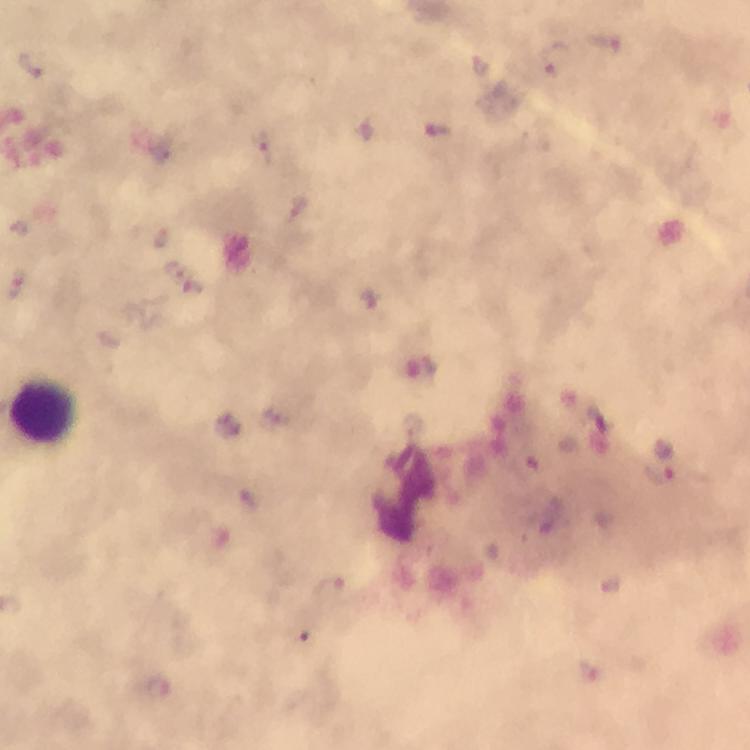

Approximate centers as (x, y) in pixels.
Summary:
  - Plasmodium parasite locations: (606, 44), (556, 59), (30, 66), (439, 132), (265, 149), (184, 279), (369, 300), (423, 368), (662, 475), (331, 588), (158, 692)
  - Leukocyte locations: (46, 411)
  - Magnification: 100x
  - Cropped from: a single field of view
  - Image size: 750×750 pixels
  - Capture: smartphone camera through the microscope
  - Preparation: thick blood smear
  - Immersion oil: used
  - Stain: Giemsa
  - Context: from a diagnostic examination for malaria